Report the malaria status of this cell.
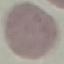
It is uninfected.

stain = Giemsa
capture = smartphone camera at the microscope eyepiece
preparation = thin smear
image type = cell patch, automatically extracted from a larger field of view and resized to 64 × 64 pixels